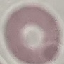
Malaria status: uninfected. Thin blood smear. Cell patch, automatically extracted from a larger field of view and resized to 64 × 64 pixels. Giemsa-stained preparation. Acquired by smartphone through the microscope eyepiece.